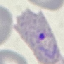

Summary:
  - Result: malaria parasites identified
  - Capture: smartphone through the microscope eyepiece
  - Stain: Giemsa
  - Preparation: thin blood film
  - Image type: cell patch, automatically extracted from a larger field of view and resized to 64 × 64 pixels